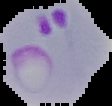

image size = 112×106 pixels
image type = cell region segmented out of the field of view; surrounding area masked to black
result = malaria parasites detected
preparation = thin blood film